Identify the parasite.
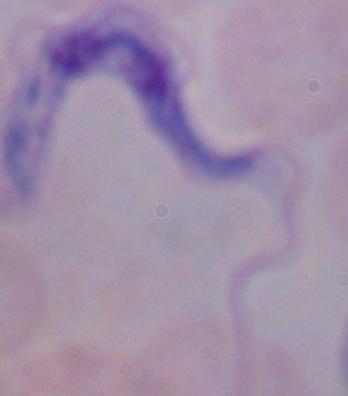

This is a trypanosome.

Photomicrograph. 1000x magnification.